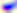

Summary:
  - Magnification: 400x
  - Modality: micrograph
  - Identification: Toxoplasma gondii